Classify this cell by malaria status.
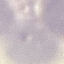
Uninfected.

Summary:
  - Preparation: thin blood film
  - Image type: automatically extracted cell patch, resized to 64 × 64 pixels
  - Capture: smartphone through the microscope eyepiece
  - Stain: Giemsa